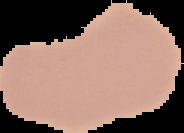

image size = 184×133 pixels
result = no Plasmodium parasites seen
preparation = thin blood smear
image type = segmented cell region with the area outside set to black